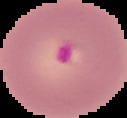

image size = 127×118 pixels
result = Plasmodium parasites detected
preparation = thin blood film
image type = segmented cell region with the area outside set to black